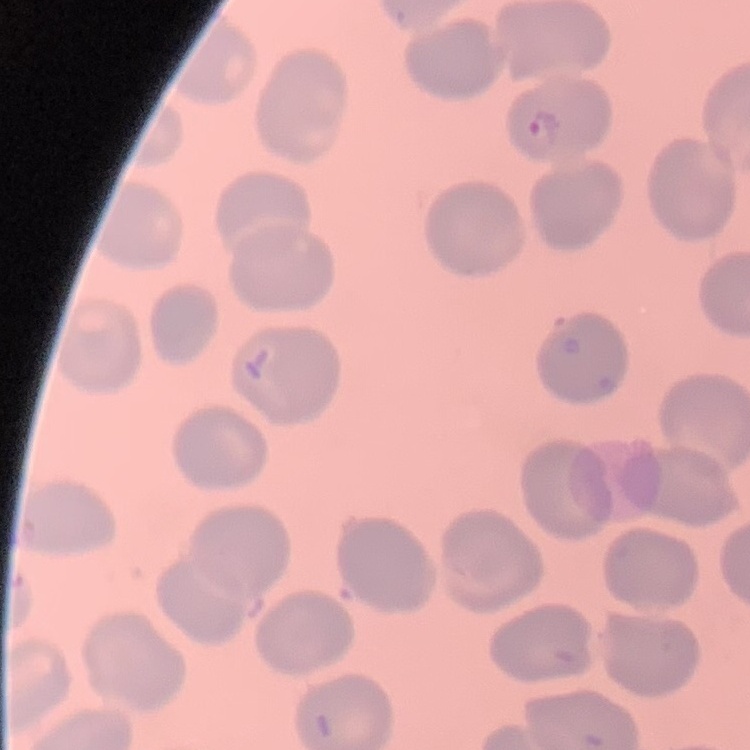
erythrocyte_morphology: no rouleaux formation
preparation: thin blood smear
stain: Field's or Giemsa
image_type: square crop of a larger photomicrograph